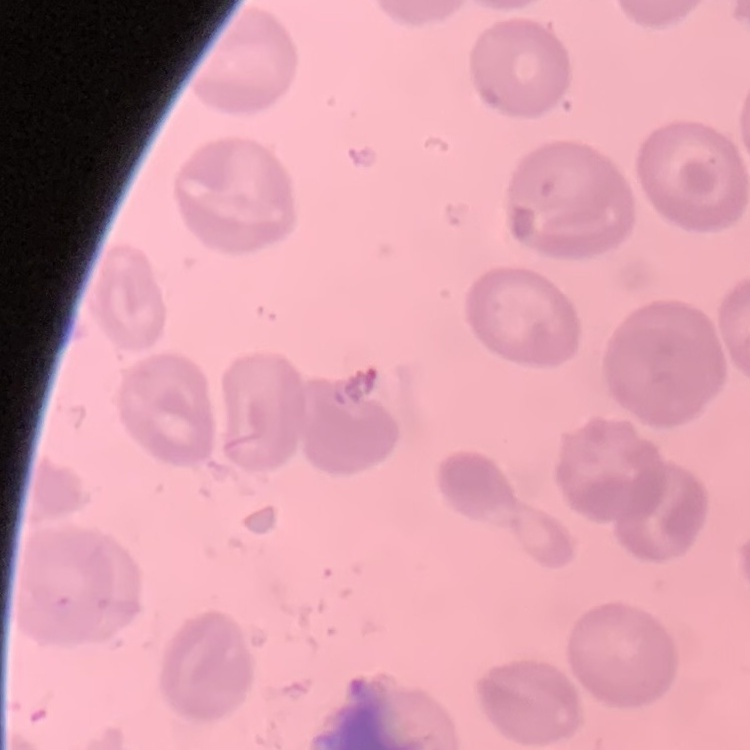

Summary:
  - Red blood cell morphology: no rouleaux formation
  - Stain: Field's or Giemsa
  - Preparation: thin blood film
  - Image type: square crop of a larger photomicrograph